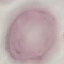

Malaria status: uninfected. Photographed with a smartphone camera at the microscope eyepiece. Automatically extracted cell patch, resized to 64 × 64 pixels. Thin blood smear. Giemsa-stained preparation.